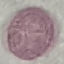
{
  "result": "no malaria parasites detected",
  "preparation": "thin blood smear",
  "stain": "Giemsa",
  "image_type": "cell patch, automatically extracted from a larger field of view and resized to 64 × 64 pixels",
  "capture": "smartphone camera at the microscope eyepiece"
}